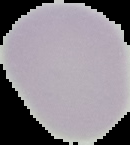

The area outside the segmented cell region is set to black. Image is 130×145 pixels. Result: no malaria parasites seen. From a thin blood smear.